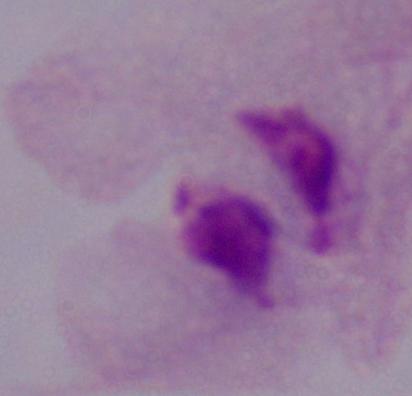

Captured at 1000x magnification. A trichomonad is shown. Micrograph.